Describe the morphology of the red blood cells.
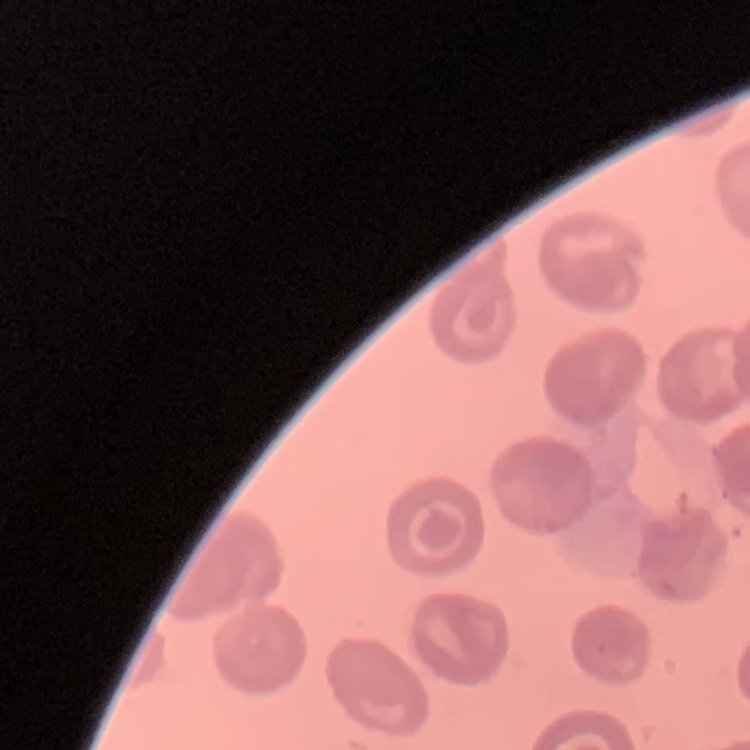
No rouleaux formation.

stain: Field's or Giemsa
preparation: thin peripheral smear
image_type: square crop of a larger photomicrograph